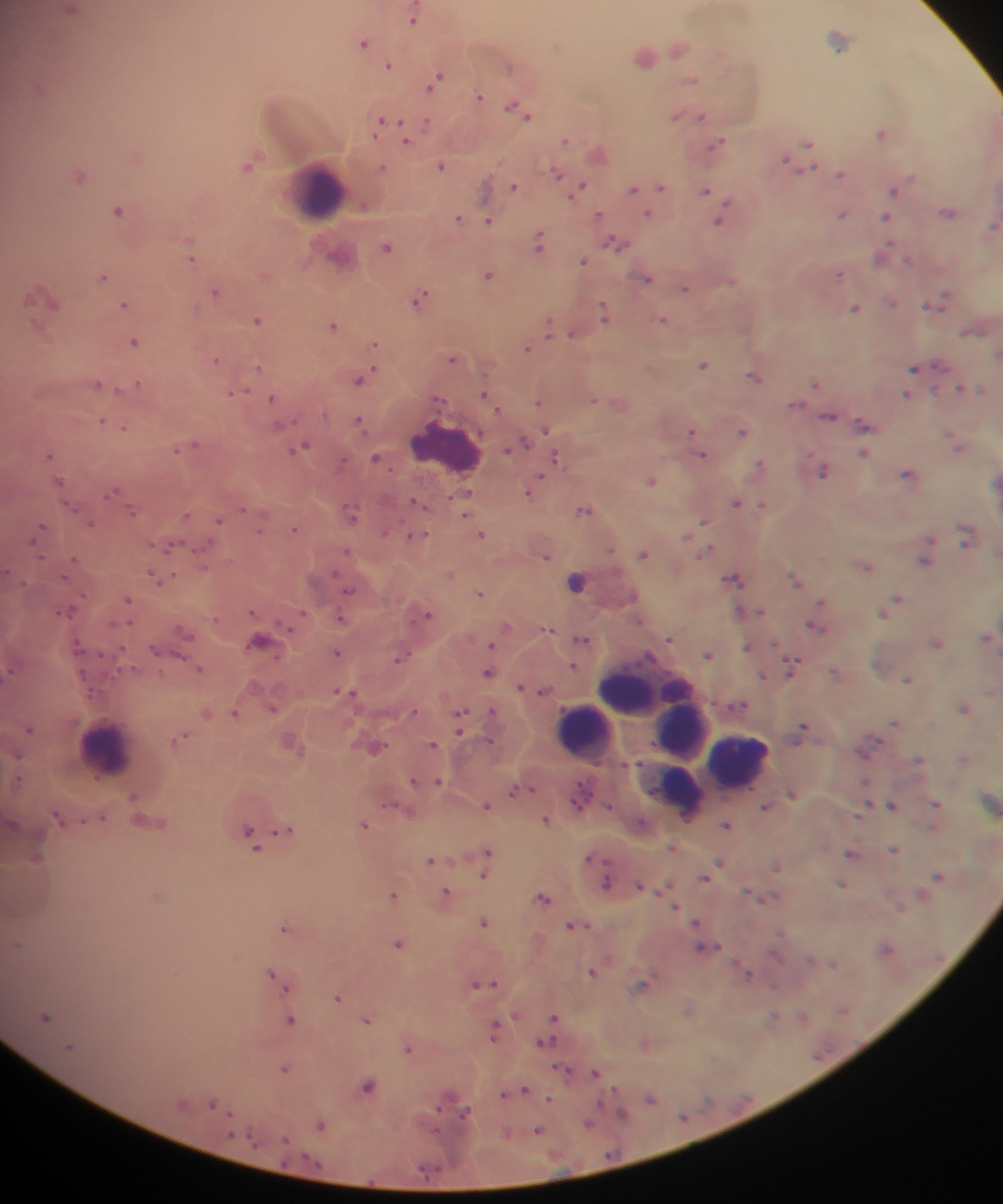

Approximate centers as x y in pixels.
Summary:
  - Malaria parasite locations: 71 10; 412 19; 838 40; 362 42; 677 49; 644 56; 388 65; 508 65; 436 80; 690 80; 479 96; 514 107; 527 115; 675 116; 701 116; 379 122; 426 124; 880 133; 405 138; 564 141; 716 143; 807 144; 785 159; 248 164; 440 165; 380 167; 806 168; 555 172; 839 173; 79 176; 513 186; 659 186; 579 187; 632 188; 704 190; 892 190; 363 207; 118 210; 947 213; 647 214; 841 214; 598 215; 885 217; 457 218; 720 219; 488 222; 991 228; 539 242; 615 242; 386 246; 882 254; 336 256; 192 258; 907 259; 583 261; 839 273; 487 275; 102 276; 645 278; 684 288; 215 292; 943 296; 41 299; 418 299; 935 301; 892 303; 123 304; 927 305; 855 308; 603 314; 256 320; 661 320; 547 325; 333 326; 971 332; 571 334; 133 342; 373 346; 526 349; 451 359; 215 360; 702 365; 937 365; 914 367; 258 368; 753 376; 360 379; 816 383; 96 384; 137 384; 960 388; 981 389; 233 393; 484 394; 906 395; 271 397; 437 399; 592 399; 538 400; 795 405; 828 416; 101 421; 358 422; 862 425; 279 426; 124 428; 545 429; 689 431; 742 432; 519 444; 190 445; 301 446; 510 447; 957 447; 176 450; 49 454; 863 454; 703 455; 375 458; 556 458; 759 464; 823 471; 906 474; 539 479; 650 480; 58 481; 996 482; 530 491; 112 492; 464 494; 416 502; 735 503; 762 504; 70 507; 242 508; 583 510; 132 512; 350 513; 463 514; 186 515; 218 521; 702 521; 90 523; 39 528; 260 529; 293 529; 384 533; 480 534; 417 536; 684 537; 928 539; 965 540; 169 547; 609 550; 707 550; 345 551; 643 554; 545 557; 72 559; 923 561; 203 567; 866 567; 450 574; 155 578; 170 578; 733 578; 795 580; 576 582; 348 590; 479 592; 897 598; 127 599; 67 611; 252 611; 758 611; 881 613; 427 614; 301 615; 340 618; 813 626; 548 629; 183 631; 987 638; 581 639; 669 639; 258 642; 936 644; 490 645; 745 647; 153 650; 336 653; 707 655; 178 656; 401 657; 571 667; 790 668; 199 669; 833 671; 7 672; 487 673; 762 676; 907 679; 519 687; 542 691; 345 692; 738 705; 272 709; 963 709; 411 712; 492 712; 234 713; 207 714; 460 718; 894 722; 28 728; 802 729; 459 731; 181 737; 489 741; 432 745; 374 748; 17 756; 962 758; 919 759; 412 781; 438 782; 514 791; 791 793; 133 795; 580 795; 936 804; 891 805; 390 806; 485 806; 764 806; 101 817; 56 818; 545 820; 363 825; 725 825; 284 830; 249 833; 253 842; 893 850; 486 851; 849 853; 34 858; 429 861; 718 863; 486 865; 774 866; 483 875; 937 876; 703 877; 607 883; 841 884; 639 885; 446 892; 393 895; 542 898; 674 906; 899 908; 695 921; 483 922; 571 926; 283 928; 397 944; 16 945; 701 947; 884 949; 833 964; 270 973; 591 973; 747 975; 487 983; 641 984; 476 985; 284 989; 336 998; 45 1017; 553 1017; 802 1017; 772 1019; 290 1020; 366 1021; 493 1030; 543 1043; 407 1049; 283 1069; 563 1071; 595 1074; 367 1087; 524 1090; 511 1092; 503 1094; 650 1098; 549 1100; 212 1103; 464 1113; 621 1115; 683 1118; 588 1123; 320 1125; 537 1131; 284 1139
  - Leukocyte locations: 316 189; 445 447; 641 691; 683 729; 583 730; 105 751; 740 762; 668 783
  - Field of view: single
  - Image size: 1003×1204 pixels
  - Capture: mobile-phone photograph through a microscope
  - Preparation: thick blood smear
  - Country: Ghana